Locate the cells, classifying each as a parasitized red blood cell, an uninfected red blood cell, or a white blood cell.
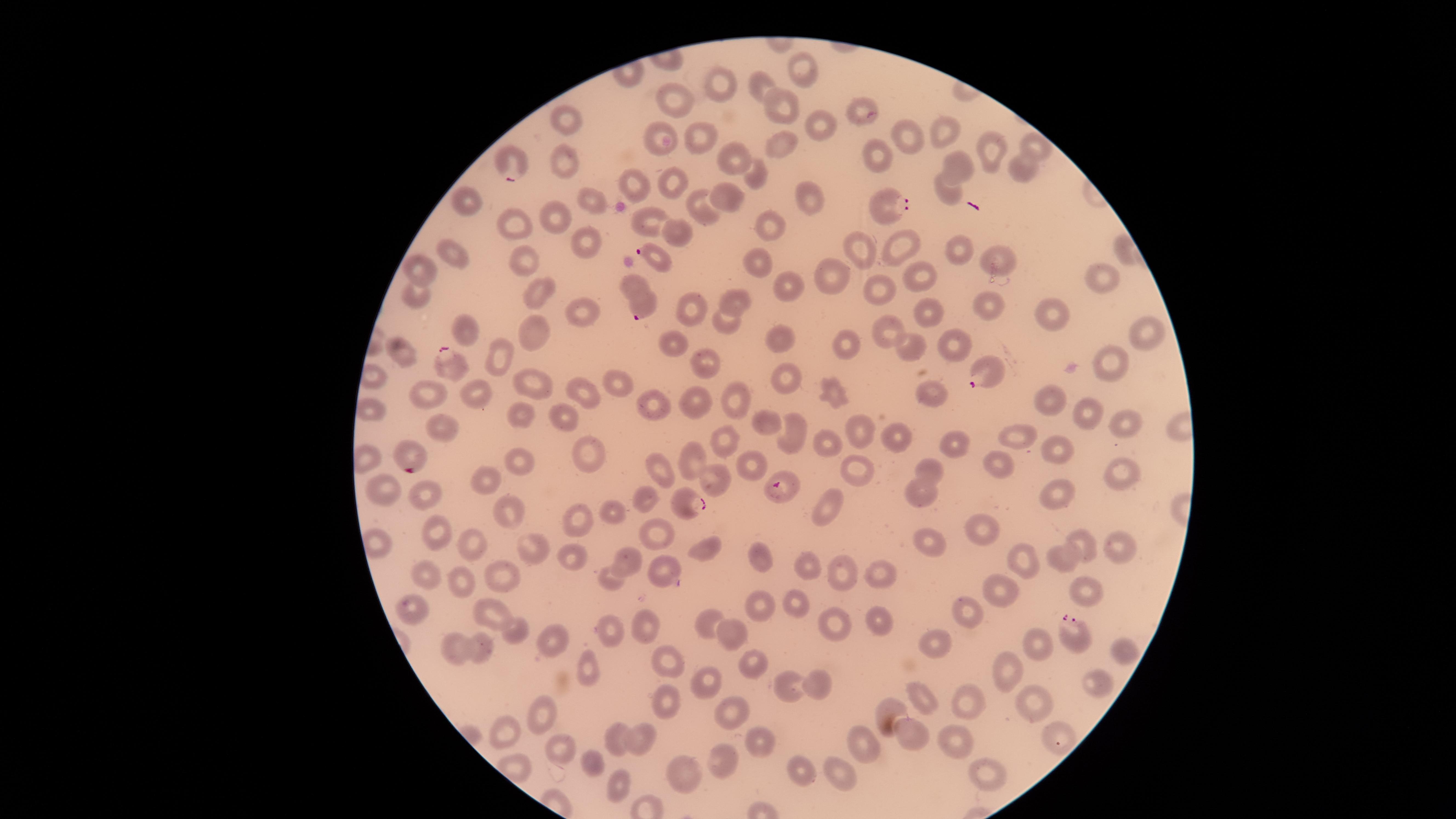
Approximate marker points, in pixels from the top-left corner.
Parasitized red blood cells: (x=508, y=166), (x=884, y=203), (x=656, y=256), (x=641, y=301), (x=450, y=358), (x=985, y=376), (x=415, y=456), (x=783, y=485), (x=692, y=506), (x=1074, y=633).
Uninfected red blood cells: (x=803, y=67), (x=760, y=81), (x=716, y=83), (x=677, y=95), (x=780, y=105), (x=858, y=106), (x=820, y=121), (x=566, y=122), (x=944, y=125), (x=658, y=131), (x=700, y=136), (x=904, y=137), (x=1033, y=144), (x=781, y=145), (x=992, y=153), (x=564, y=155), (x=732, y=158), (x=868, y=158), (x=959, y=164), (x=1020, y=171), (x=755, y=175), (x=638, y=180), (x=668, y=180), (x=947, y=191), (x=468, y=197), (x=730, y=197), (x=810, y=199), (x=594, y=201), (x=707, y=211), (x=645, y=214), (x=556, y=215), (x=512, y=225), (x=773, y=225), (x=677, y=229), (x=579, y=240), (x=861, y=247), (x=898, y=248), (x=957, y=249), (x=452, y=253), (x=1000, y=255), (x=521, y=259), (x=761, y=261), (x=422, y=266), (x=836, y=271), (x=913, y=272), (x=1101, y=277), (x=632, y=282), (x=786, y=284), (x=884, y=289), (x=537, y=292), (x=419, y=294), (x=736, y=296), (x=986, y=306), (x=578, y=308), (x=694, y=309), (x=1055, y=311), (x=921, y=312), (x=724, y=320), (x=890, y=326), (x=463, y=329), (x=537, y=331), (x=783, y=335), (x=1141, y=335), (x=950, y=340), (x=673, y=341), (x=844, y=344), (x=912, y=347), (x=404, y=351), (x=701, y=357), (x=504, y=358), (x=1107, y=362), (x=785, y=367), (x=526, y=380), (x=618, y=382), (x=428, y=390), (x=825, y=391), (x=586, y=393), (x=932, y=394), (x=1053, y=396), (x=482, y=397), (x=733, y=399), (x=652, y=402), (x=701, y=403), (x=369, y=408), (x=1090, y=414), (x=523, y=415), (x=566, y=417), (x=764, y=419), (x=1120, y=422), (x=441, y=425), (x=795, y=426), (x=861, y=429), (x=899, y=437), (x=827, y=438), (x=1019, y=438), (x=723, y=440), (x=958, y=442), (x=1055, y=445), (x=589, y=453), (x=699, y=461), (x=746, y=461), (x=1001, y=461), (x=524, y=462), (x=656, y=463), (x=929, y=467), (x=861, y=471), (x=1118, y=471), (x=492, y=479), (x=717, y=480), (x=384, y=493), (x=425, y=493), (x=645, y=493), (x=918, y=494), (x=1055, y=499), (x=826, y=506), (x=513, y=509), (x=608, y=510), (x=577, y=522), (x=982, y=526), (x=651, y=528), (x=436, y=535), (x=930, y=538), (x=1115, y=542), (x=1078, y=543), (x=471, y=544), (x=700, y=546), (x=531, y=547), (x=571, y=554), (x=759, y=557), (x=1023, y=558), (x=1064, y=560), (x=629, y=561), (x=807, y=563), (x=664, y=568), (x=844, y=573), (x=878, y=573), (x=507, y=575), (x=426, y=576), (x=610, y=576), (x=454, y=580), (x=1007, y=589), (x=1084, y=589), (x=794, y=599), (x=757, y=604), (x=964, y=606), (x=411, y=607), (x=489, y=608), (x=876, y=617), (x=706, y=624), (x=832, y=624), (x=643, y=626), (x=515, y=629), (x=613, y=631), (x=730, y=632), (x=551, y=637), (x=937, y=642), (x=480, y=646), (x=1036, y=646), (x=457, y=647), (x=1117, y=649), (x=669, y=661), (x=755, y=665), (x=587, y=668), (x=1008, y=669), (x=701, y=677), (x=1095, y=680), (x=813, y=681), (x=788, y=689), (x=671, y=698), (x=924, y=698), (x=962, y=699), (x=1033, y=699), (x=892, y=709), (x=729, y=713), (x=544, y=717), (x=951, y=731), (x=907, y=736), (x=863, y=737), (x=760, y=738), (x=506, y=739), (x=645, y=739), (x=1059, y=739), (x=621, y=740), (x=557, y=745), (x=598, y=759), (x=726, y=766), (x=800, y=770), (x=987, y=771), (x=685, y=773), (x=838, y=775), (x=610, y=780).
No white blood cells identified.

Summary:
  - Visible region: circular
  - Stain: Giemsa
  - Image size: 1456×819 pixels
  - Species: Plasmodium falciparum
  - Capture: smartphone photograph through the microscope eyepiece
  - Preparation: thin blood film
  - Field of view: single